Comment on the morphology of the erythrocytes.
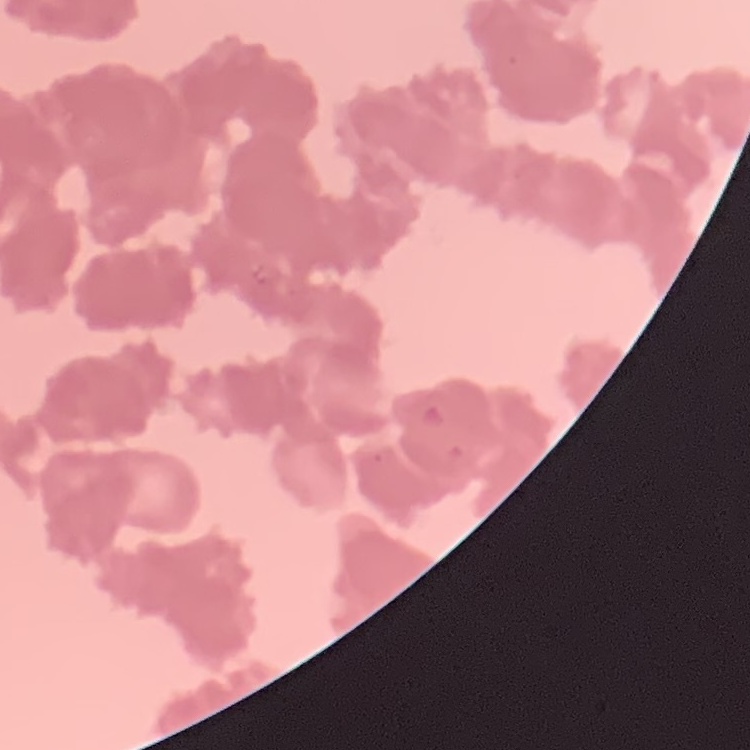
They show rouleaux formation.

stain = Field's or Giemsa
image type = square crop of a larger photomicrograph
preparation = thin peripheral smear